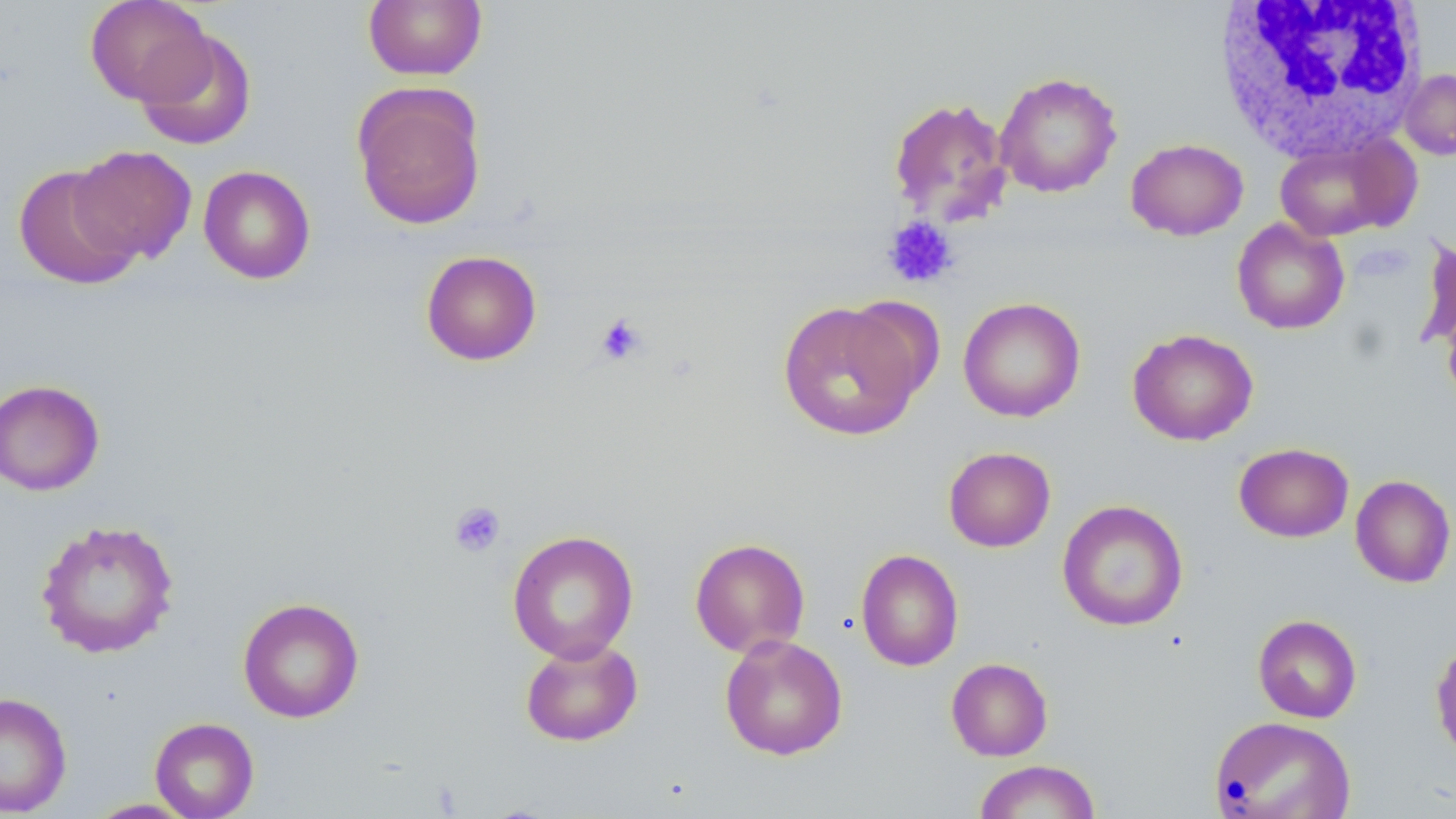

Summary:
  - Coordinate format: approximate bounding boxes as [x1, y1, x2, y2] in pixels
  - Platelet locations: [883, 216, 957, 288], [593, 312, 647, 366], [448, 501, 506, 557]
  - Uninfected red blood cell locations: [84, 0, 214, 106], [362, 0, 488, 81], [136, 28, 257, 151], [1399, 69, 1456, 160], [994, 72, 1122, 198], [351, 83, 487, 230], [887, 95, 1013, 225], [1273, 135, 1413, 242], [1126, 138, 1248, 240], [70, 145, 197, 265], [13, 163, 142, 290], [198, 165, 316, 284], [1231, 218, 1350, 335], [1416, 236, 1456, 352], [420, 250, 542, 366], [958, 296, 1085, 422], [778, 300, 925, 442], [1127, 328, 1258, 446], [0, 378, 105, 496], [1233, 442, 1354, 543], [942, 446, 1056, 552], [1350, 474, 1455, 588], [1057, 499, 1189, 632], [35, 518, 179, 659], [507, 530, 639, 663], [689, 537, 811, 657], [855, 549, 964, 671], [237, 596, 365, 723], [1253, 614, 1362, 723], [719, 634, 848, 761], [520, 638, 644, 747], [1430, 641, 1456, 764], [945, 657, 1053, 761], [0, 691, 72, 816], [1209, 716, 1356, 818], [149, 717, 259, 819], [973, 760, 1101, 818], [84, 798, 200, 818]
  - White blood cell locations: [1212, 1, 1430, 164]
  - Slide-level diagnosis: no evidence of blood parasites
  - Field of view: one of a larger specimen
  - Modality: optical microscopy
  - Magnification: 1000x
  - Stain: May-Grünwald-Giemsa
  - Image size: 1456×819 pixels
  - Preparation: thin blood smear